Assess the morphology of the erythrocytes.
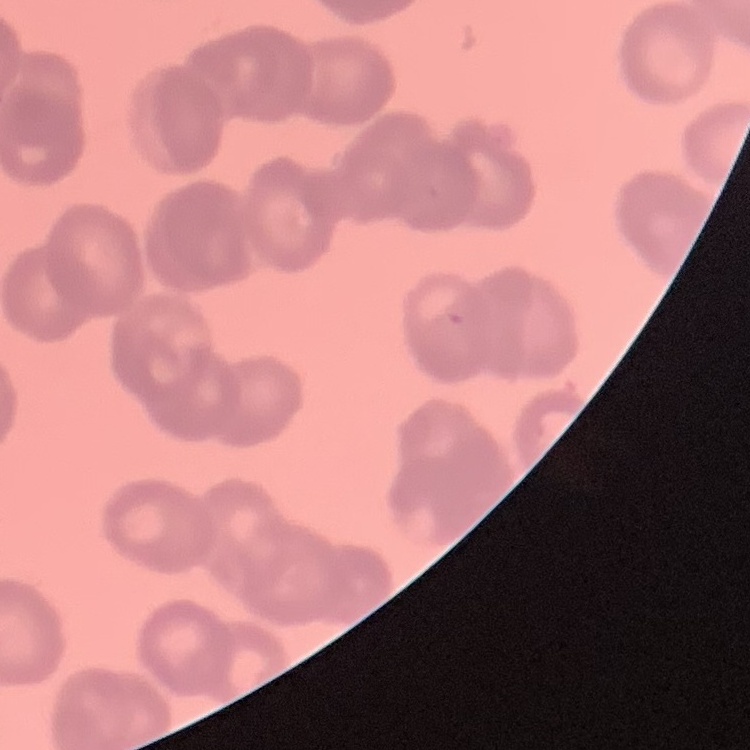

Rouleaux formation.

Field's or Giemsa stain. One tile cut from a larger photomicrograph. Thin blood film.